Comment on the morphology of the erythrocytes.
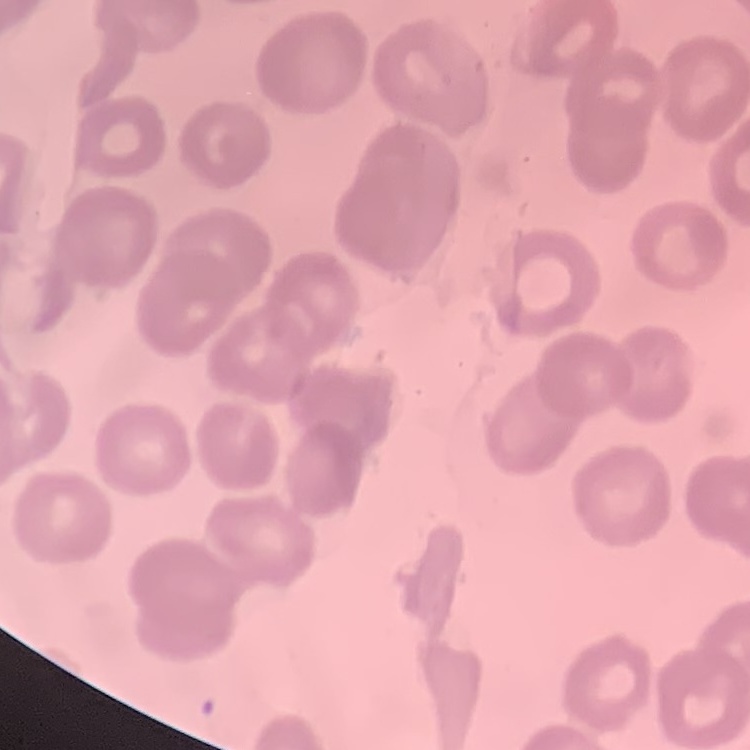
No rouleaux formation.

Summary:
  - Preparation: thin blood film
  - Stain: Field's or Giemsa
  - Image type: one tile cut from a larger photomicrograph